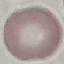

Summary:
  - Malaria status: uninfected
  - Stain: Giemsa
  - Capture: smartphone camera at the microscope eyepiece
  - Preparation: thin blood smear
  - Image type: automatically extracted cell patch, resized to 64 × 64 pixels